Classify this cell by malaria status.
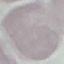

It is uninfected.

Summary:
  - Capture: smartphone camera at the microscope eyepiece
  - Image type: cell patch, automatically extracted from a larger field of view and resized to 64 × 64 pixels
  - Preparation: thin blood smear
  - Stain: Giemsa